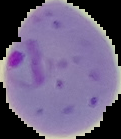
Summary:
  - Result: malaria parasites identified
  - Preparation: thin blood film
  - Image type: cell region segmented out of the field of view; surrounding area masked to black
  - Image size: 121×139 pixels